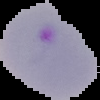
Image is 100×100 pixels. Segmented cell region on a black background. Malaria status: parasitized. From a thin blood film.